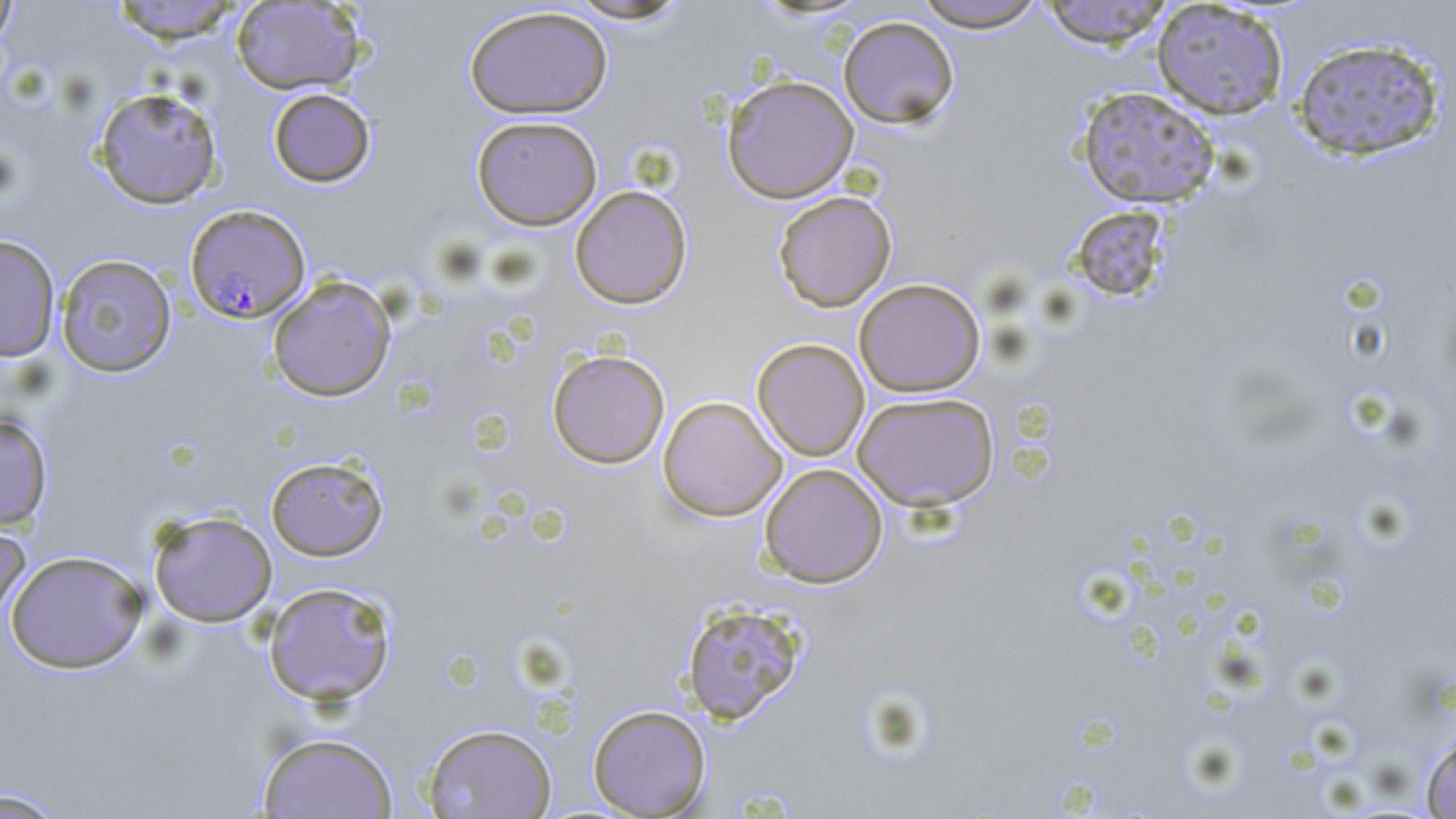

slide_level_diagnosis: Plasmodium falciparum
image_size: 1456×819 pixels
preparation: thin blood film
uninfected_red_blood_cell_locations: 'approximate bounding boxes as [x1, y1, x2, y2] in pixels: [0, 0, 19, 53], [108, 0, 246, 43], [566, 0, 693, 24], [911, 0, 1050, 32], [1040, 0, 1174, 48], [231, 1, 365, 95], [252, 1, 369, 187], [1151, 1, 1289, 120], [464, 5, 613, 119], [838, 15, 960, 129], [1292, 36, 1446, 161], [722, 75, 859, 203], [1076, 85, 1221, 209], [92, 86, 224, 209], [267, 88, 376, 188], [471, 115, 602, 229], [569, 185, 692, 309], [772, 190, 897, 312], [1070, 204, 1173, 309], [0, 234, 61, 363], [55, 253, 177, 378], [268, 276, 396, 402], [854, 278, 985, 397], [752, 338, 869, 461], [547, 349, 670, 469], [852, 391, 1000, 511], [657, 396, 787, 521], [0, 413, 53, 530], [265, 455, 388, 561], [759, 463, 888, 588], [148, 510, 278, 627], [0, 521, 31, 628], [5, 550, 148, 674], [263, 581, 397, 706], [680, 600, 806, 724], [588, 704, 711, 817], [423, 723, 558, 819], [257, 732, 399, 818], [1420, 733, 1456, 818], [0, 787, 69, 818]'
plasmodium_falciparum_infected_red_blood_cell_locations: 'approximate bounding boxes as [x1, y1, x2, y2] in pixels: [185, 204, 310, 323]'
field_of_view: one of a larger specimen
stain: May-Grünwald-Giemsa
modality: light microscopy
magnification: 1000x